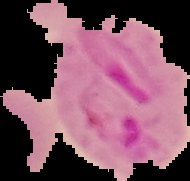

The area outside the segmented cell region is set to black. From a thin blood smear. Result: Plasmodium parasites identified. Image is 190×181 pixels.